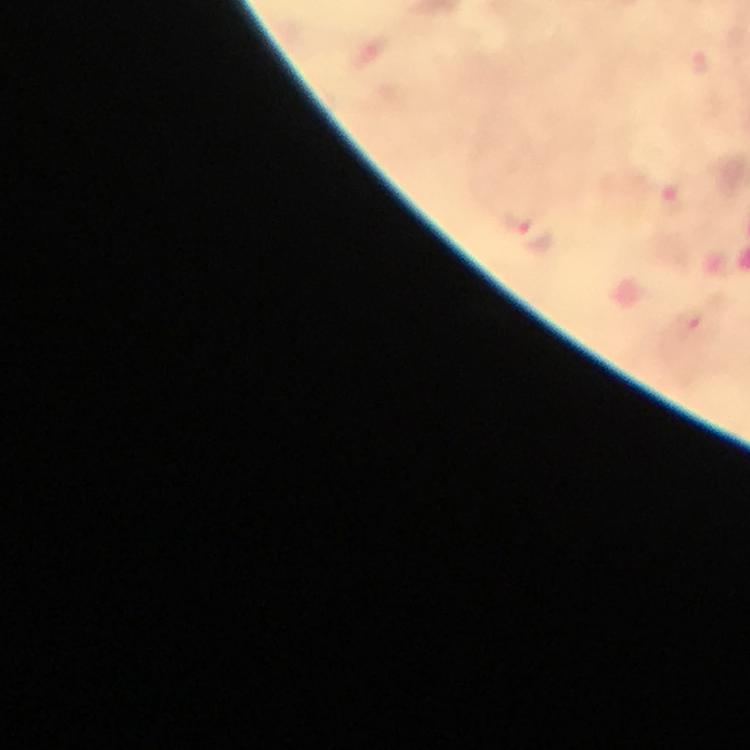

Plasmodium parasite locations = approximate centers as [x, y] in pixels: [519, 219]
immersion oil = applied
stain = Giemsa
context = from a diagnostic examination for malaria
cropped from = one field of view
magnification = 100x
preparation = thick blood film
capture = smartphone camera through the microscope
image size = 750×750 pixels